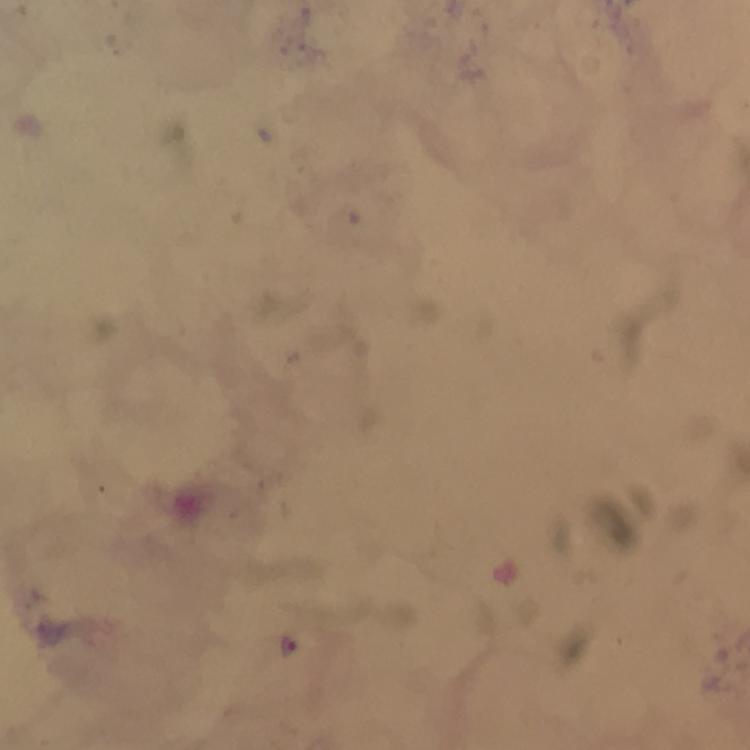 Approximate object centers, in pixels from the top-left corner. Malaria parasite locations: (x=290, y=644). Immersion oil was used. A crop from one field of view. Giemsa stain. Thick blood film. Photographed with a smartphone mounted on the microscope. From a malaria diagnostic workup. Image is 750×750 pixels. At 100x magnification.